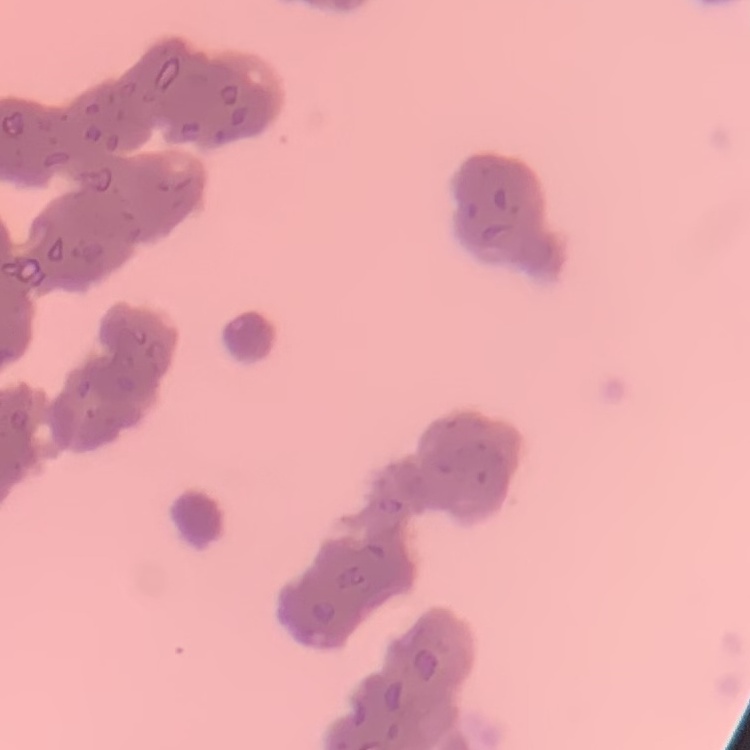
red blood cell morphology = rouleaux formation
stain = Field's or Giemsa
preparation = thin blood smear
image type = one tile cut from a larger photomicrograph